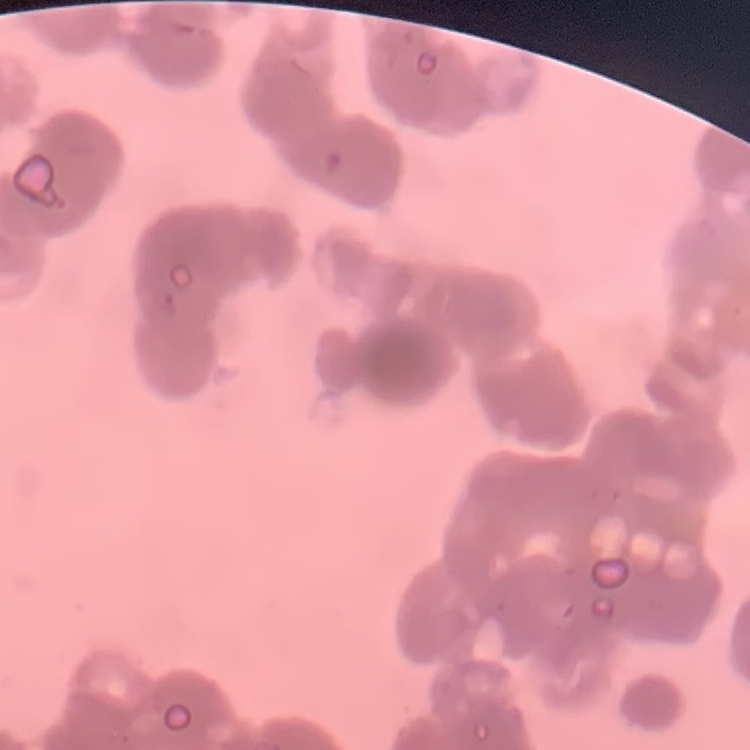 The red blood cells exhibit rouleaux formation. Stained with either Field's or Giemsa. Thin blood smear. One tile cut from a larger photomicrograph.